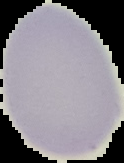

From a thin blood smear. Malaria status: uninfected. The area outside the segmented cell region is set to black. Image is 124×163 pixels.